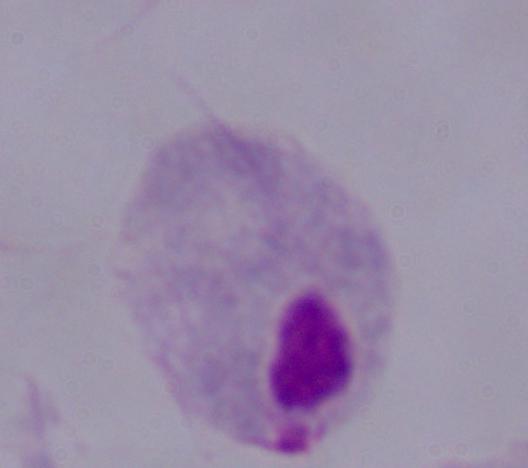
identification = trichomonad
magnification = 1000x
modality = micrograph